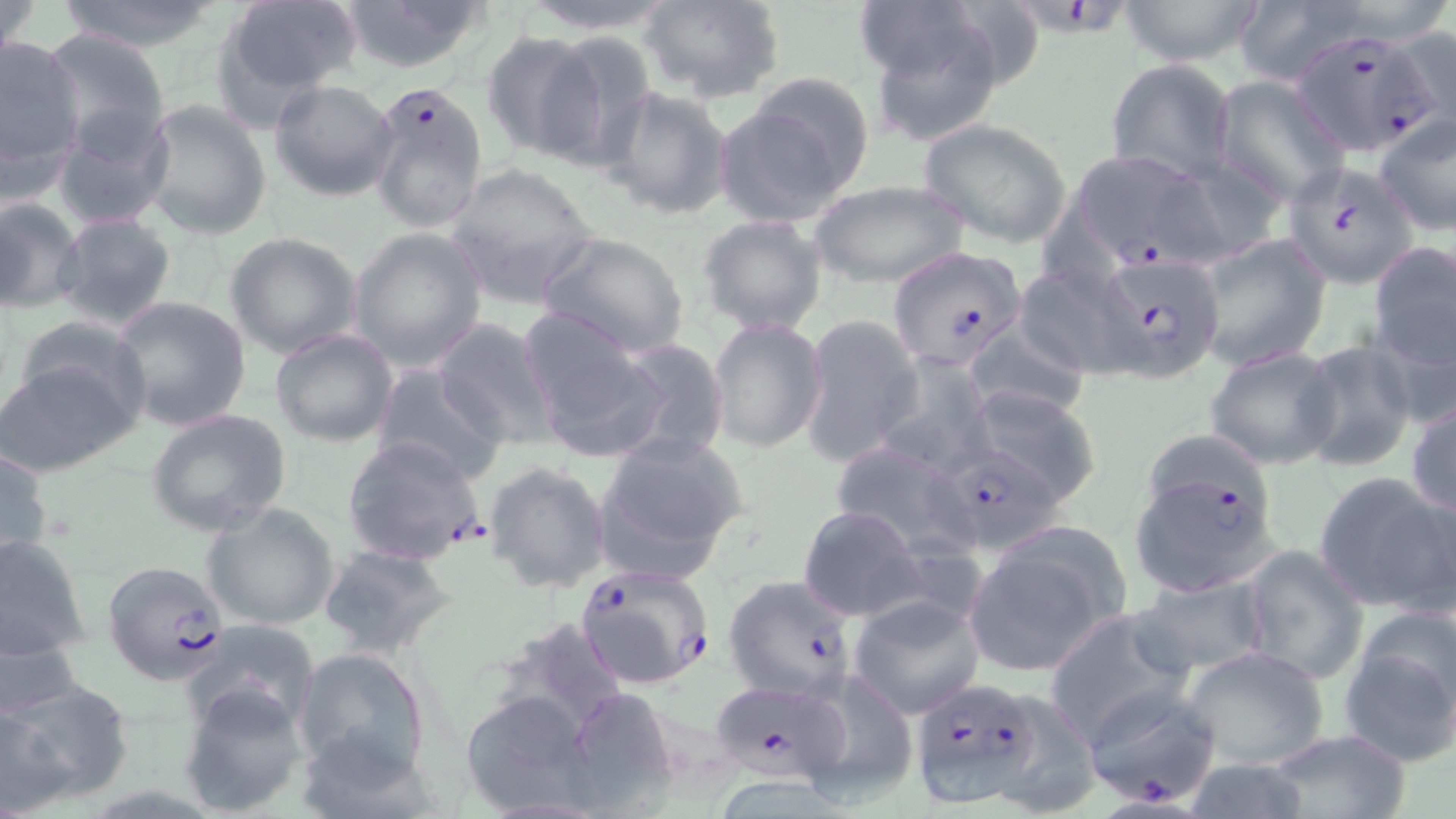
Summary:
  - Coordinate format: approximate bounding boxes as (x1, y1, x2, y2) in pixels
  - Plasmodium falciparum-infected red blood cell locations (subset): (1026, 0, 1137, 43), (1292, 33, 1450, 156), (368, 80, 491, 234), (1067, 150, 1216, 269), (1286, 161, 1416, 287), (885, 244, 1027, 370), (1098, 256, 1224, 381), (342, 437, 486, 566), (918, 445, 1067, 559), (103, 561, 230, 684), (574, 563, 716, 691), (722, 573, 858, 704), (706, 679, 856, 787), (910, 680, 1051, 808), (1080, 685, 1226, 811)
  - Uninfected red blood cell locations (subset): (0, 0, 46, 59), (56, 0, 225, 52), (212, 0, 363, 118), (338, 0, 491, 72), (511, 0, 680, 34), (639, 0, 784, 105), (1119, 0, 1262, 67), (863, 8, 1013, 144), (1381, 26, 1455, 143), (37, 28, 171, 153), (480, 30, 604, 160), (534, 30, 660, 167), (0, 32, 88, 184), (1106, 57, 1237, 183), (743, 69, 877, 195), (1213, 77, 1348, 205), (268, 79, 400, 202), (602, 87, 734, 220), (712, 97, 856, 226), (140, 99, 271, 241), (52, 106, 174, 231), (1373, 116, 1455, 237), (917, 118, 1073, 247), (1155, 155, 1287, 268), (443, 162, 600, 307), (811, 180, 969, 289), (0, 195, 84, 315), (52, 211, 179, 332), (697, 214, 829, 337), (348, 226, 487, 372), (536, 230, 690, 358), (225, 231, 362, 359), (1195, 234, 1332, 371), (1366, 242, 1455, 375), (1014, 263, 1142, 379), (1325, 272, 1441, 454), (109, 296, 253, 433), (521, 313, 664, 459), (11, 315, 152, 433), (799, 315, 921, 467), (432, 317, 559, 447), (707, 317, 828, 453), (959, 320, 1092, 422), (271, 328, 397, 446), (610, 339, 731, 463), (1296, 342, 1420, 471), (1204, 345, 1339, 469), (0, 351, 140, 476), (872, 353, 997, 479), (368, 362, 509, 486), (966, 385, 1101, 506), (1407, 395, 1456, 519), (146, 409, 292, 540), (594, 433, 748, 581), (827, 441, 979, 561), (0, 445, 52, 573), (484, 461, 611, 594), (1313, 470, 1456, 616), (203, 500, 341, 629), (797, 506, 925, 622), (0, 531, 92, 667), (962, 532, 1123, 676), (1240, 543, 1370, 686), (317, 545, 457, 660), (1128, 575, 1272, 681), (847, 595, 985, 719), (1043, 607, 1199, 747), (186, 620, 323, 733), (1341, 623, 1456, 771), (1180, 645, 1331, 771), (292, 647, 431, 781), (793, 671, 921, 806), (1, 678, 132, 811), (177, 681, 308, 816), (563, 686, 679, 814), (459, 689, 599, 816), (1260, 727, 1413, 819), (1177, 758, 1318, 817)
  - Slide-level diagnosis: Plasmodium falciparum
  - Magnification: 1000x
  - Field of view: one of a larger specimen
  - Modality: light microscopy
  - Preparation: thin blood smear
  - Image size: 1456×819 pixels
  - Stain: May-Grünwald-Giemsa